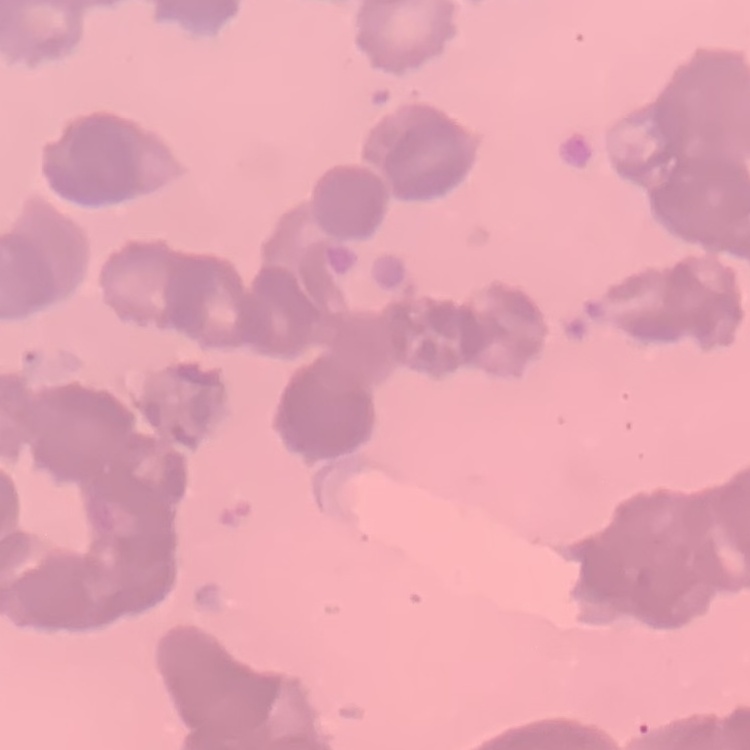

erythrocyte morphology = rouleaux formation
preparation = thin blood smear
image type = one tile cut from a larger photomicrograph
stain = Field's or Giemsa